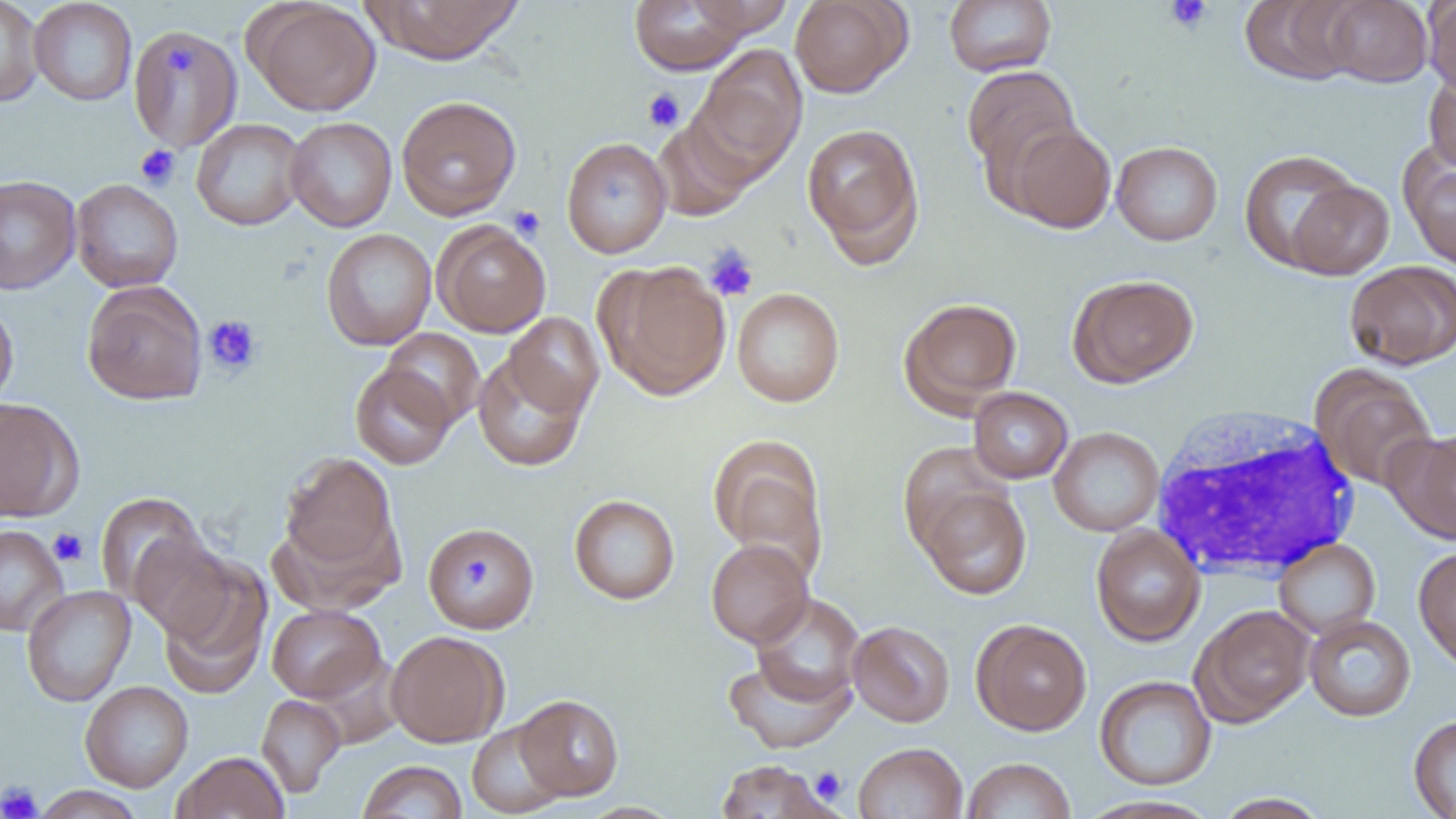
Approximate bounding boxes as named x1/y1/x2/y2 corners in pixels. Platelet locations: (x1=1164, y1=0, x2=1212, y2=33), (x1=165, y1=43, x2=198, y2=76), (x1=642, y1=88, x2=685, y2=132), (x1=135, y1=144, x2=181, y2=190), (x1=509, y1=206, x2=546, y2=241), (x1=704, y1=246, x2=759, y2=302), (x1=203, y1=315, x2=262, y2=377), (x1=48, y1=527, x2=89, y2=567), (x1=463, y1=551, x2=494, y2=594), (x1=810, y1=766, x2=848, y2=804), (x1=0, y1=781, x2=42, y2=819). Uninfected red blood cell locations: (x1=0, y1=0, x2=44, y2=107), (x1=28, y1=0, x2=138, y2=106), (x1=245, y1=0, x2=382, y2=116), (x1=363, y1=0, x2=526, y2=65), (x1=629, y1=0, x2=750, y2=75), (x1=686, y1=0, x2=794, y2=37), (x1=790, y1=0, x2=910, y2=98), (x1=944, y1=0, x2=1056, y2=76), (x1=1239, y1=0, x2=1365, y2=85), (x1=1322, y1=0, x2=1433, y2=87), (x1=1423, y1=1, x2=1456, y2=97), (x1=129, y1=25, x2=244, y2=154), (x1=692, y1=45, x2=808, y2=179), (x1=962, y1=65, x2=1082, y2=188), (x1=1423, y1=70, x2=1456, y2=174), (x1=396, y1=95, x2=521, y2=220), (x1=285, y1=116, x2=397, y2=232), (x1=652, y1=116, x2=755, y2=221), (x1=191, y1=118, x2=307, y2=231), (x1=802, y1=122, x2=925, y2=264), (x1=1006, y1=123, x2=1117, y2=233), (x1=561, y1=137, x2=671, y2=258), (x1=1111, y1=141, x2=1223, y2=246), (x1=1400, y1=141, x2=1456, y2=273), (x1=1239, y1=149, x2=1360, y2=271), (x1=0, y1=174, x2=80, y2=295), (x1=70, y1=178, x2=184, y2=293), (x1=1286, y1=179, x2=1394, y2=280), (x1=432, y1=220, x2=551, y2=338), (x1=321, y1=228, x2=436, y2=350), (x1=1345, y1=260, x2=1456, y2=370), (x1=597, y1=261, x2=732, y2=400), (x1=1068, y1=274, x2=1199, y2=387), (x1=82, y1=280, x2=207, y2=406), (x1=731, y1=288, x2=845, y2=406), (x1=898, y1=296, x2=1022, y2=414), (x1=0, y1=299, x2=18, y2=412), (x1=503, y1=312, x2=604, y2=418), (x1=381, y1=327, x2=485, y2=428), (x1=473, y1=351, x2=589, y2=472), (x1=350, y1=363, x2=457, y2=469), (x1=1312, y1=367, x2=1437, y2=492), (x1=968, y1=387, x2=1073, y2=484), (x1=0, y1=397, x2=83, y2=522), (x1=1049, y1=426, x2=1164, y2=536), (x1=1391, y1=429, x2=1456, y2=544), (x1=708, y1=435, x2=829, y2=577), (x1=897, y1=440, x2=1011, y2=554), (x1=280, y1=452, x2=400, y2=578), (x1=918, y1=484, x2=1031, y2=600), (x1=94, y1=491, x2=208, y2=606), (x1=568, y1=494, x2=680, y2=605), (x1=423, y1=519, x2=540, y2=630), (x1=0, y1=525, x2=69, y2=636), (x1=1091, y1=525, x2=1205, y2=647), (x1=129, y1=535, x2=238, y2=642), (x1=706, y1=538, x2=813, y2=647), (x1=1273, y1=538, x2=1380, y2=638), (x1=1413, y1=546, x2=1456, y2=672), (x1=158, y1=557, x2=271, y2=698), (x1=21, y1=585, x2=136, y2=707), (x1=750, y1=592, x2=865, y2=708), (x1=266, y1=604, x2=385, y2=703), (x1=1192, y1=604, x2=1315, y2=726), (x1=1304, y1=615, x2=1416, y2=721), (x1=971, y1=619, x2=1092, y2=735), (x1=847, y1=620, x2=956, y2=727), (x1=386, y1=630, x2=509, y2=747), (x1=722, y1=654, x2=856, y2=754), (x1=1095, y1=675, x2=1216, y2=790), (x1=80, y1=680, x2=193, y2=792), (x1=256, y1=694, x2=345, y2=798), (x1=513, y1=694, x2=625, y2=800), (x1=1408, y1=715, x2=1456, y2=818), (x1=467, y1=720, x2=568, y2=818), (x1=853, y1=742, x2=967, y2=818), (x1=172, y1=751, x2=289, y2=819), (x1=961, y1=757, x2=1075, y2=819), (x1=713, y1=759, x2=838, y2=818), (x1=357, y1=760, x2=468, y2=819), (x1=33, y1=785, x2=145, y2=819), (x1=1212, y1=793, x2=1332, y2=819), (x1=1076, y1=795, x2=1222, y2=819). White blood cell locations: (x1=1149, y1=407, x2=1365, y2=581). Slide-level diagnosis: no evidence of blood parasites. Thin blood film. 1000x magnification. Image is 1456×819 pixels. Single field of view. Optical microscopy.